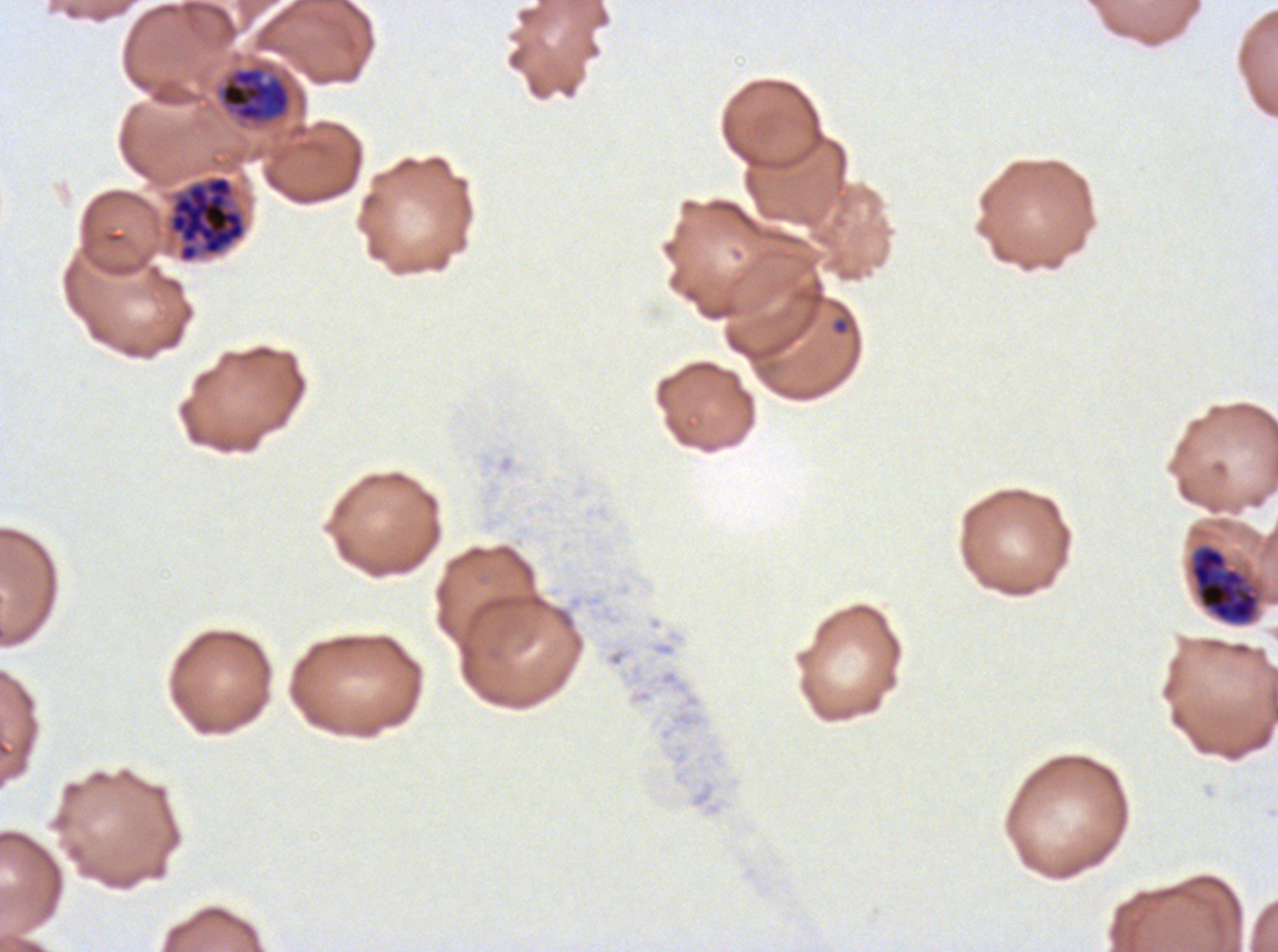

notation = approximate bounding rectangles given as corner coordinates in pixels from the top-left
late schizont locations = (x1=168, y1=175, x2=246, y2=262)
late trophozoite locations = (x1=218, y1=67, x2=291, y2=124)
early schizont locations = (x1=1189, y1=544, x2=1260, y2=625)
ring locations = (x1=830, y1=315, x2=851, y2=336)
preparation = thin blood smear
life-cycle stages observed = ring, late trophozoite, early schizont, late schizont
image size = 1278×952 pixels
stain = Giemsa
specimen = Plasmodium falciparum cultured ex vivo for 24 to 48 hours, from a patient in The Gambia
field of view = sub-image separated from a larger composite